Assess the morphology of the erythrocytes.
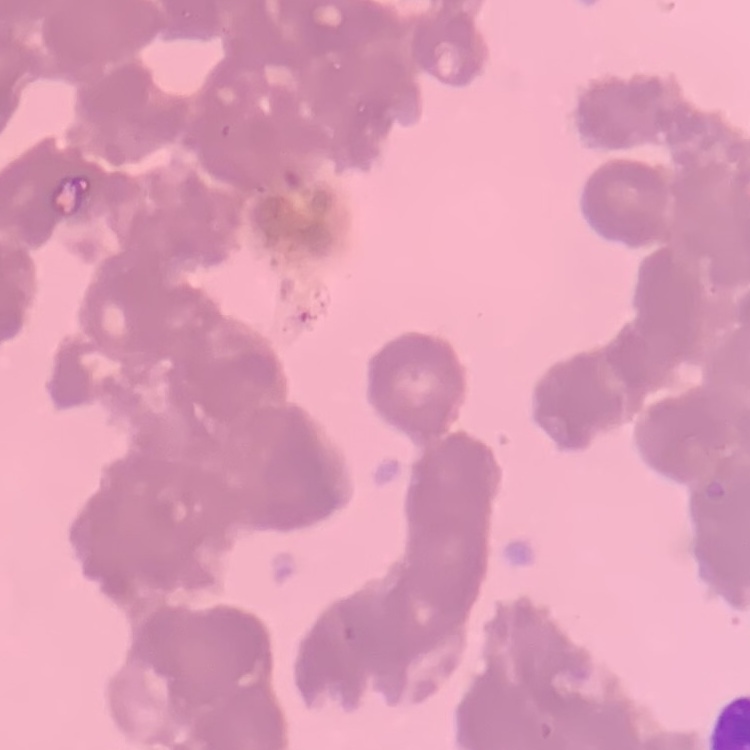

Rouleaux formation.

Thin peripheral smear. One tile cut from a larger photomicrograph. Stained with either Field's or Giemsa.